Describe the morphology of the red blood cells.
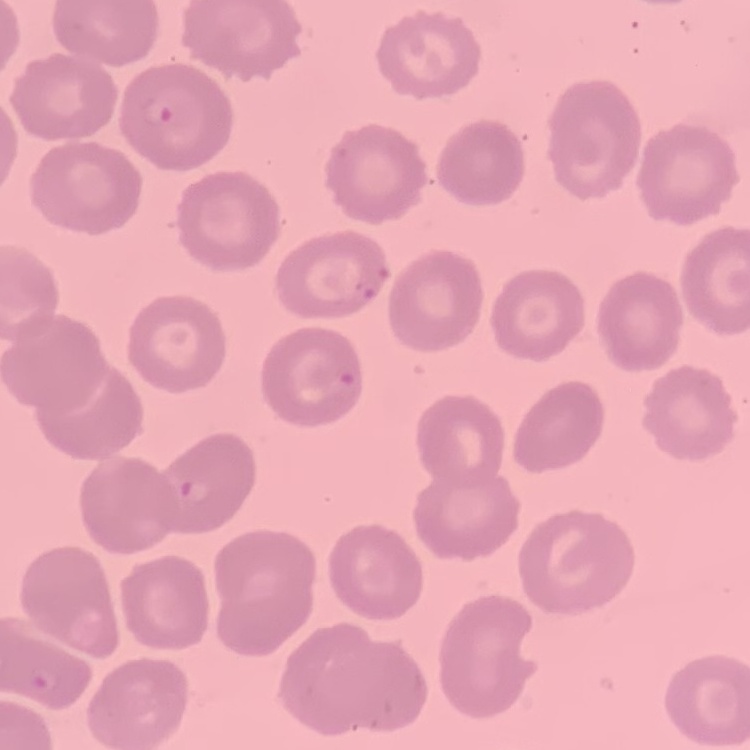

They show no rouleaux formation.

image type = square crop of a larger photomicrograph
preparation = thin peripheral smear
stain = Field's or Giemsa